Outline Plasmodium falciparum parasites and classify them by life-cycle stage.
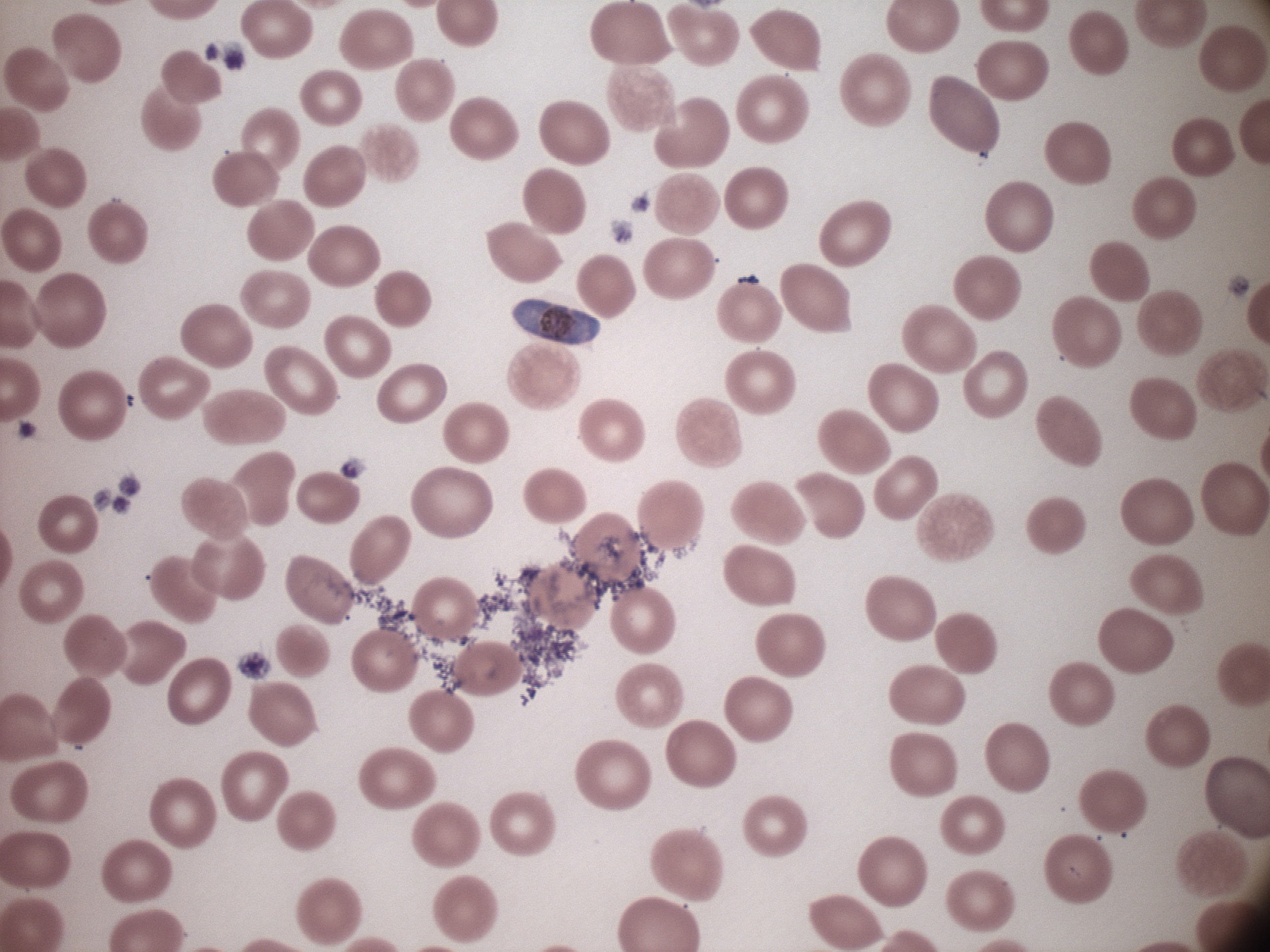
Approximate bounding boxes as named x1/y1/x2/y2 corners in pixels, from the source annotation, which is not necessarily exhaustive.
Gametocytes: (x1=513, y1=299, x2=600, y2=345).

Thin blood smear. Giemsa-stained preparation. Acquired with a Leica DM2000 optical microscope and its built-in camera. 100x magnification. Image is 1270×952 pixels. Species: Plasmodium falciparum. Single field of view.